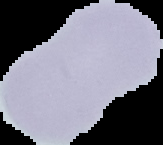
image size = 163×145 pixels
image type = segmented cell region on a black background
preparation = thin blood film
malaria status = uninfected